Comment on the morphology of the erythrocytes.
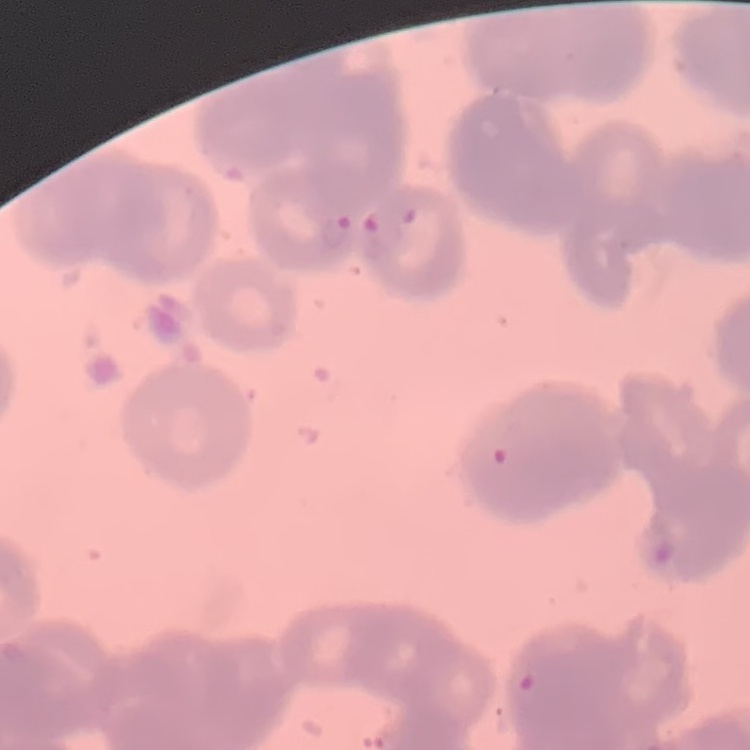

Rouleaux formation.

{
  "stain": "Field's or Giemsa",
  "image_type": "square crop of a larger photomicrograph",
  "preparation": "thin blood film"
}